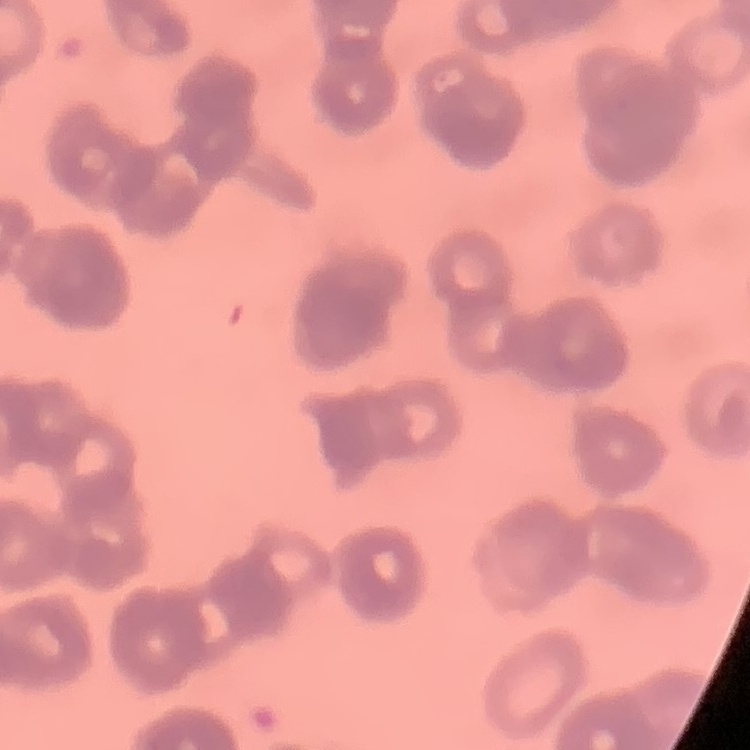

erythrocyte morphology = rouleaux formation
stain = Field's or Giemsa
preparation = thin blood film
image type = square crop of a larger photomicrograph